Identify the preparation type.
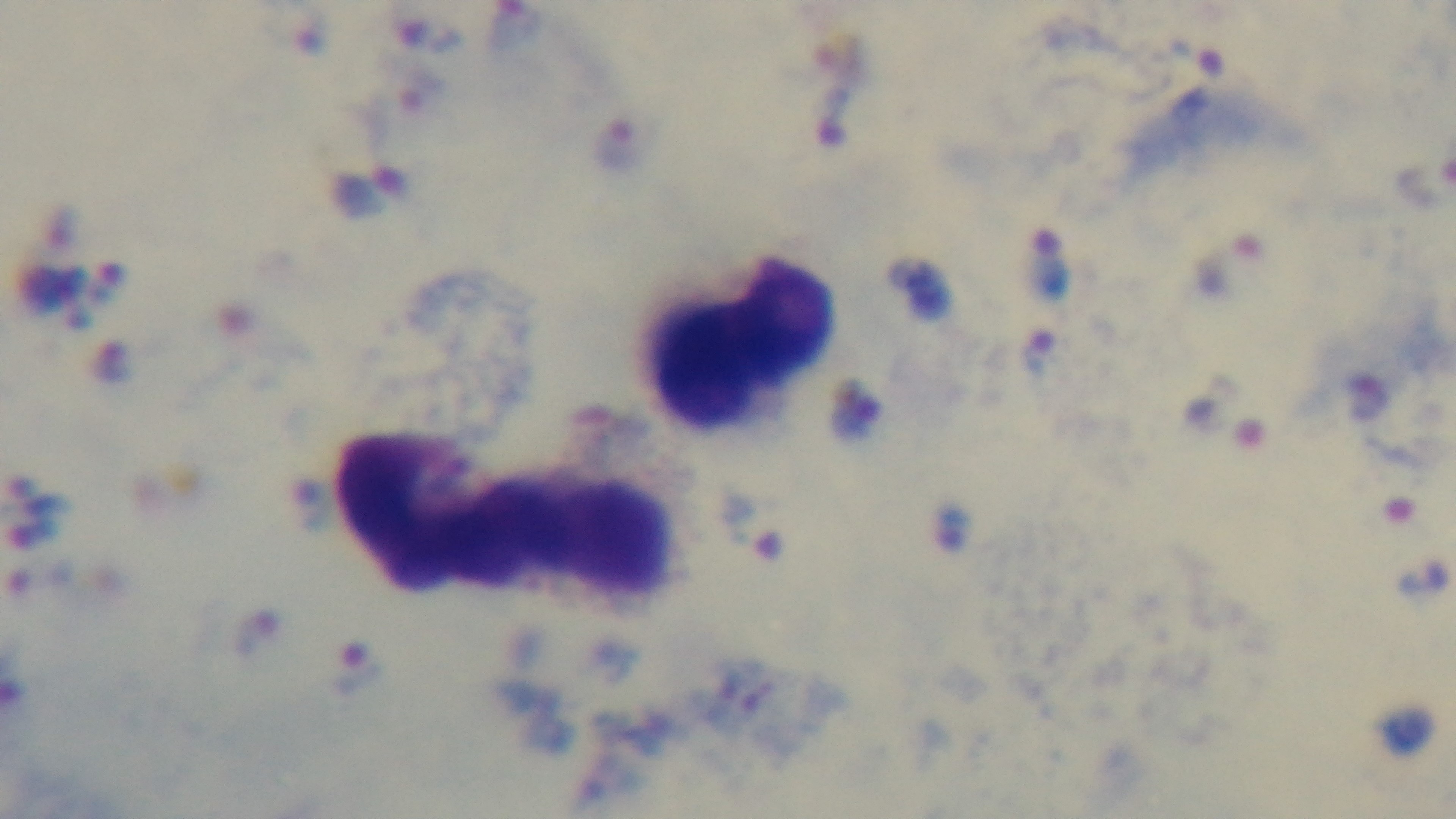

Thick.

malaria status = infected
objective = 100x oil immersion
modality = light microscopy
stain = Giemsa
field of view = single
capture = mounted 4K digital camera